Outline each uninfected red blood cell.
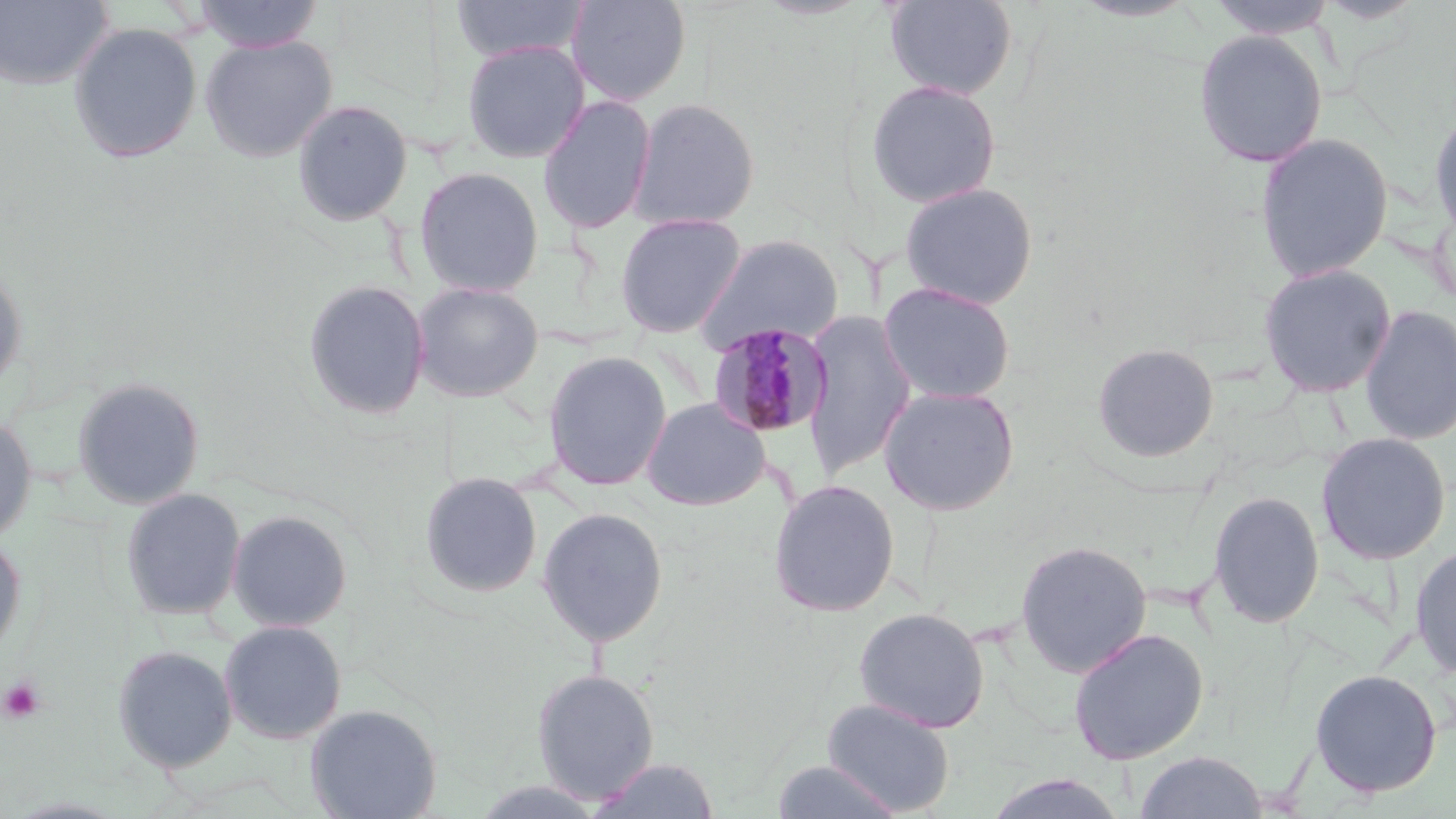
Approximate bounding boxes as (x1,y1)-(x2,y2) corner pairs in pixels.
Uninfected red blood cells: (0,0)-(114,91), (193,0)-(325,53), (451,0)-(588,62), (566,0)-(692,106), (884,0)-(1018,100), (1204,0)-(1340,38), (68,22)-(203,164), (1193,28)-(1328,168), (200,34)-(338,162), (461,40)-(590,163), (865,78)-(1003,208), (537,95)-(657,234), (627,97)-(761,231), (291,99)-(413,227), (1427,100)-(1456,248), (1254,132)-(1394,283), (413,166)-(545,297), (898,181)-(1040,310), (615,212)-(746,338), (692,234)-(845,354), (1257,263)-(1397,398), (0,265)-(27,394), (302,279)-(431,420), (411,281)-(545,402), (877,281)-(1017,404), (1358,304)-(1455,446), (801,310)-(917,480), (1091,342)-(1220,463), (542,351)-(672,491), (72,376)-(205,509), (878,385)-(1021,516), (640,397)-(771,510), (0,412)-(37,543), (1315,432)-(1452,565), (419,471)-(543,599), (767,479)-(901,618), (121,487)-(246,621), (1207,491)-(1325,629), (536,507)-(669,647), (226,509)-(353,632), (0,531)-(26,662), (1015,539)-(1153,678), (1410,544)-(1456,680), (853,606)-(990,733), (218,620)-(347,744), (1068,628)-(1209,765), (112,644)-(237,773), (531,668)-(660,804), (1309,668)-(1443,797), (822,698)-(956,816), (305,703)-(442,819), (1133,750)-(1269,818), (589,756)-(723,818), (770,759)-(905,819), (981,773)-(1130,819).

Platelet locations: (1,677)-(46,724). Plasmodium malariae-infected red blood cell locations: (708,323)-(834,439). Slide-level diagnosis: Plasmodium malariae. Thin blood film. 1000x magnification. One field of a larger specimen. Image is 1456×819 pixels. Optical microscopy. May-Grünwald-Giemsa-stained preparation.